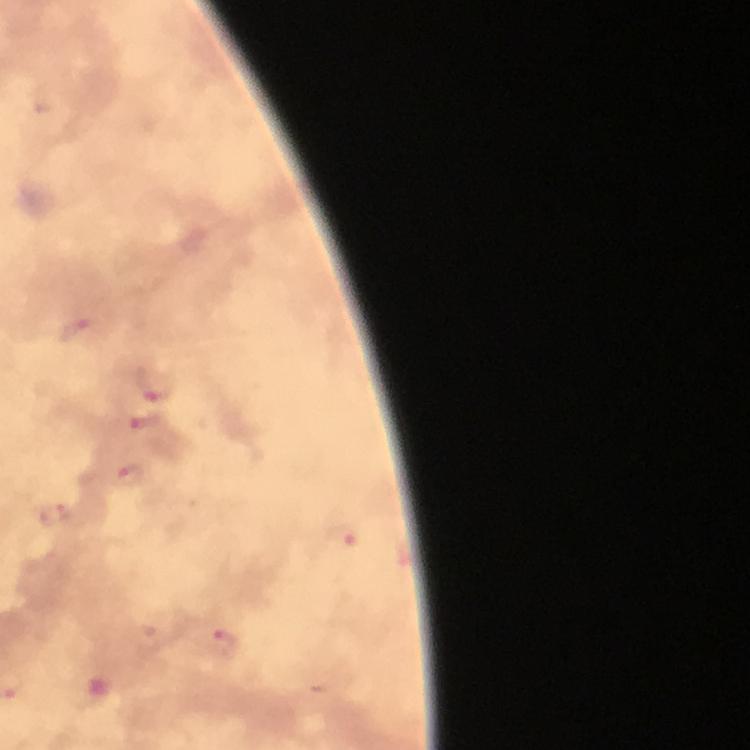

Approximate object centers, in pixels from the top-left corner.
Summary:
  - Plasmodium parasite locations: (x=73, y=328), (x=157, y=386), (x=148, y=420), (x=128, y=476), (x=223, y=644)
  - Stain: Giemsa
  - Immersion oil: used
  - Magnification: 100x
  - Context: from a diagnostic examination for malaria
  - Preparation: thick blood smear
  - Image size: 750×750 pixels
  - Capture: smartphone mounted on the microscope
  - Cropped from: one field of view